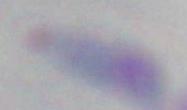
Summary:
  - Magnification: 1000x
  - Modality: photomicrograph
  - Identification: Toxoplasma gondii